Report the malaria status of this cell.
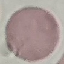

It is uninfected.

Summary:
  - Stain: Giemsa
  - Capture: smartphone through the microscope eyepiece
  - Preparation: thin blood film
  - Image type: cell patch, automatically extracted from a larger field of view and resized to 64 × 64 pixels